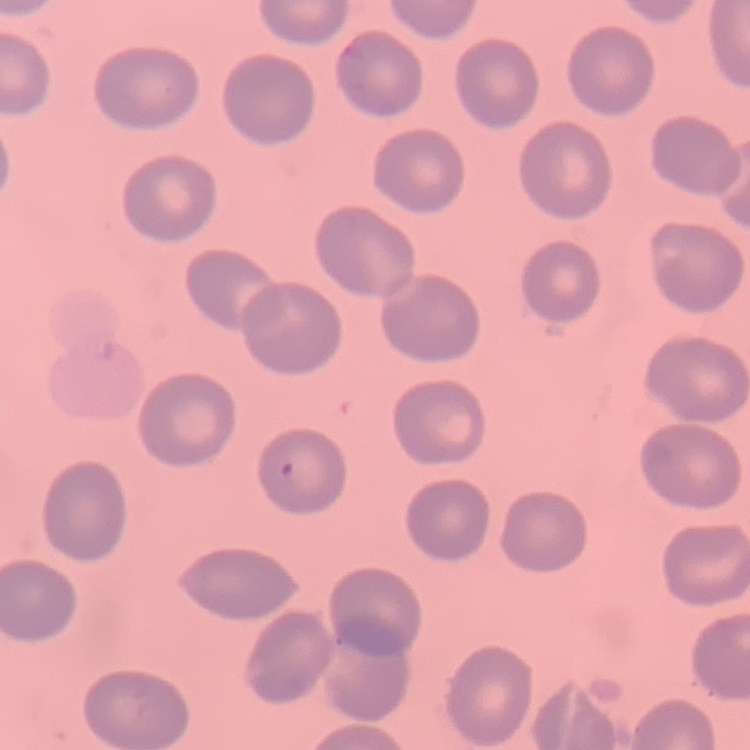
The erythrocytes show no rouleaux formation. One tile cut from a larger photomicrograph. Stained with either Field's or Giemsa. Thin peripheral smear.